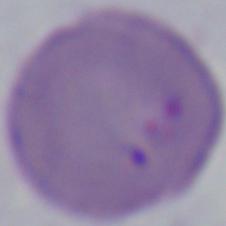
modality = micrograph
identification = Babesia
magnification = 1000x